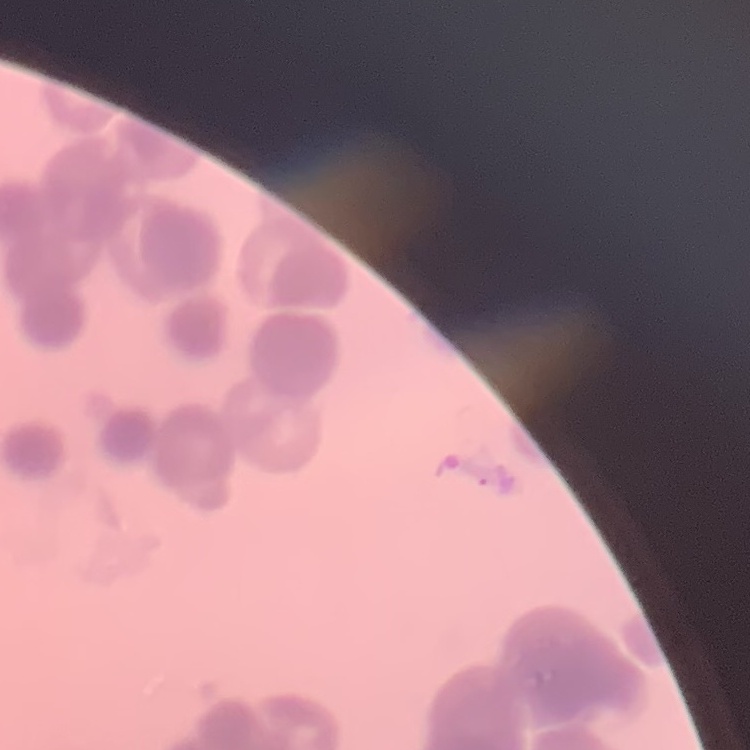
Summary:
  - Erythrocyte morphology: rouleaux formation
  - Image type: one tile cut from a larger photomicrograph
  - Preparation: thin peripheral smear
  - Stain: Field's or Giemsa